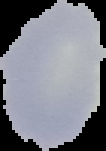

Summary:
  - Malaria status: uninfected
  - Image size: 106×151 pixels
  - Preparation: thin blood smear
  - Image type: segmented cell region with the area outside set to black